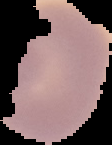 Cell region segmented out of the field of view; the surrounding area is masked to black. From a thin blood smear. Image is 112×145 pixels. Malaria status: uninfected.